Give the position of every leukocyte visible.
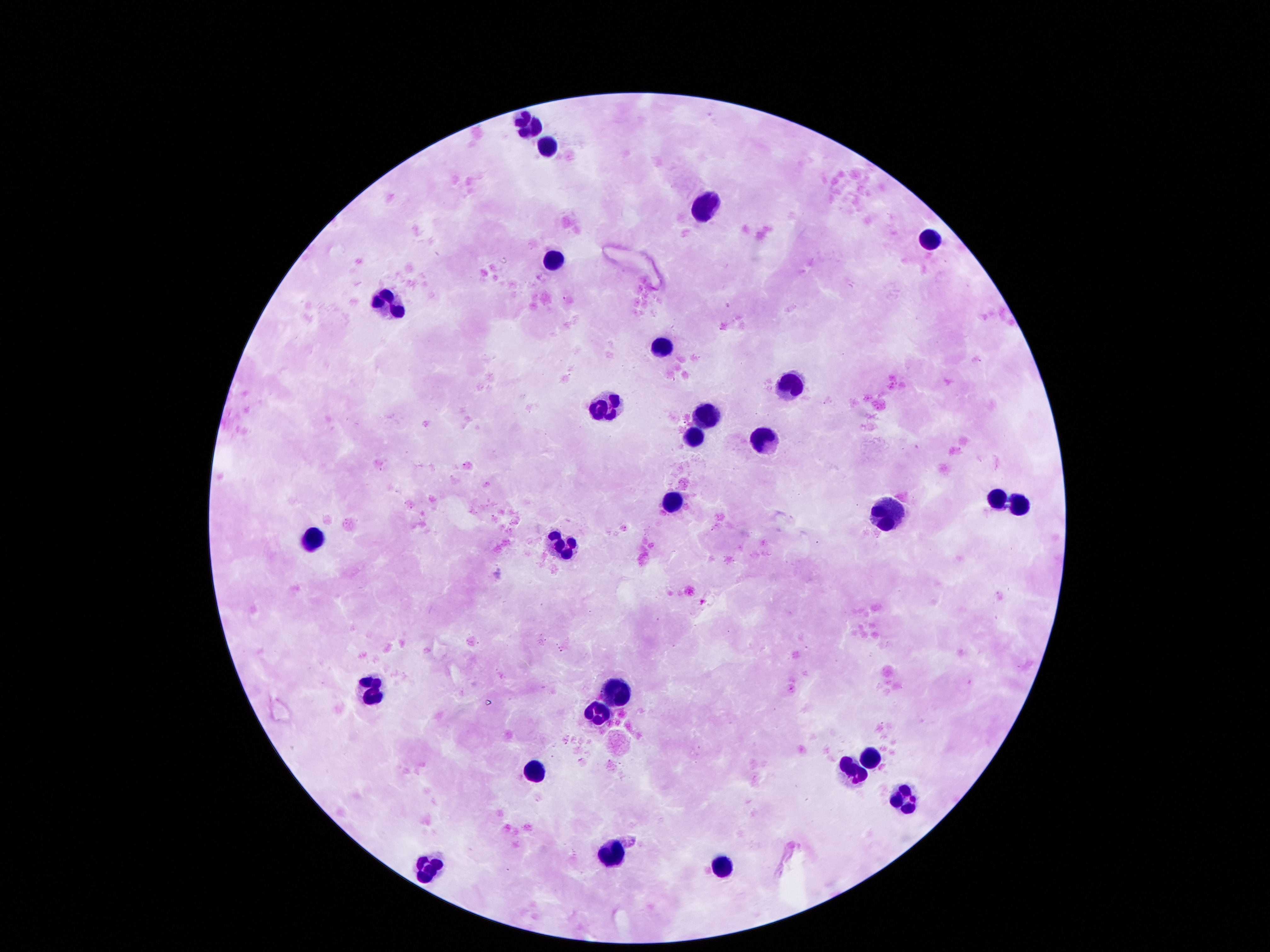
Approximate centers as {x, y} in pixels.
Leukocytes: {524, 125}, {547, 142}, {706, 201}, {932, 236}, {554, 256}, {389, 301}, {660, 346}, {790, 381}, {605, 402}, {709, 411}, {696, 434}, {761, 434}, {993, 498}, {667, 502}, {1016, 505}, {887, 514}, {311, 540}, {560, 544}, {618, 685}, {369, 686}, {596, 715}, {870, 754}, {531, 769}, {851, 770}, {903, 795}, {605, 853}, {719, 864}, {428, 867}.

Summary:
  - Capture: smartphone camera through the microscope eyepiece
  - Magnification: 100x
  - Stain: Giemsa
  - Image size: 1270×952 pixels
  - Field of view: single
  - Patient malaria status: not infected
  - Preparation: thick blood film